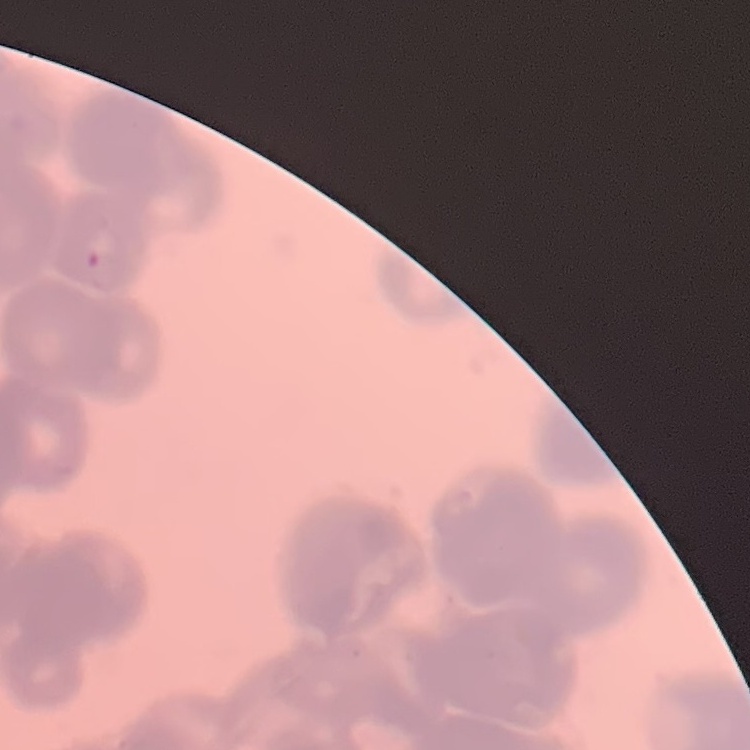
The red blood cells exhibit rouleaux formation. One tile cut from a larger photomicrograph. Stained with either Field's or Giemsa. Thin peripheral smear.